Classify this cell by malaria status.
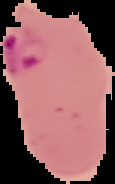
Parasitized.

Summary:
  - Image size: 115×184 pixels
  - Preparation: thin blood smear
  - Image type: cell region segmented out of the field of view; surrounding area masked to black